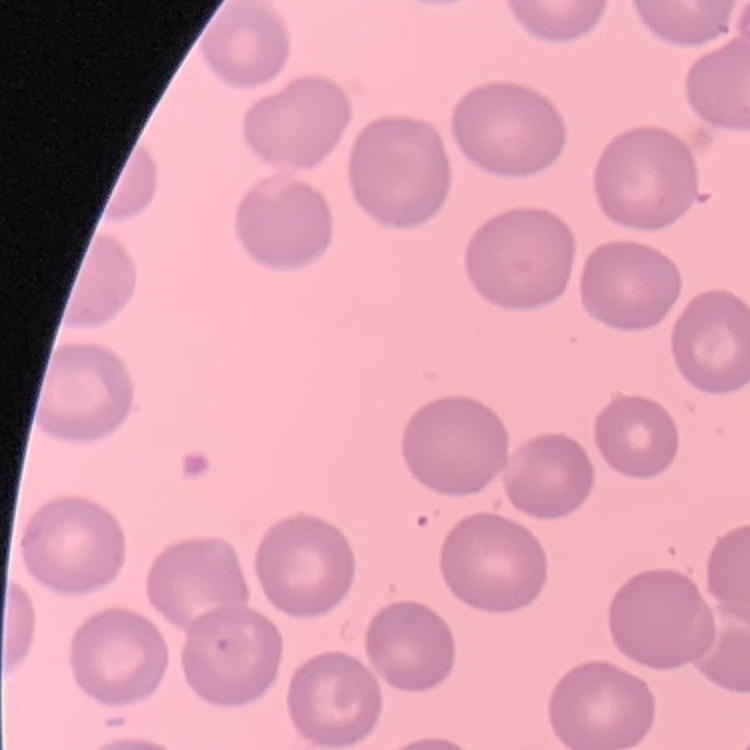
Summary:
  - Red blood cell morphology: no rouleaux formation
  - Preparation: thin blood film
  - Stain: Field's or Giemsa
  - Image type: square crop of a larger photomicrograph